Report the malaria status of this cell.
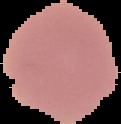
It is uninfected.

Summary:
  - Image type: cell region segmented out of the field of view; surrounding area masked to black
  - Preparation: thin blood film
  - Image size: 121×124 pixels